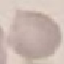
Malaria status: uninfected. Acquired by smartphone through the microscope eyepiece. Automatically extracted cell patch, resized to 64 × 64 pixels. Thin blood smear. Giemsa-stained preparation.